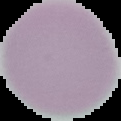
Summary:
  - Result: negative for malaria parasites
  - Preparation: thin blood film
  - Image type: segmented cell region on a black background
  - Image size: 121×121 pixels